Give the preparation type.
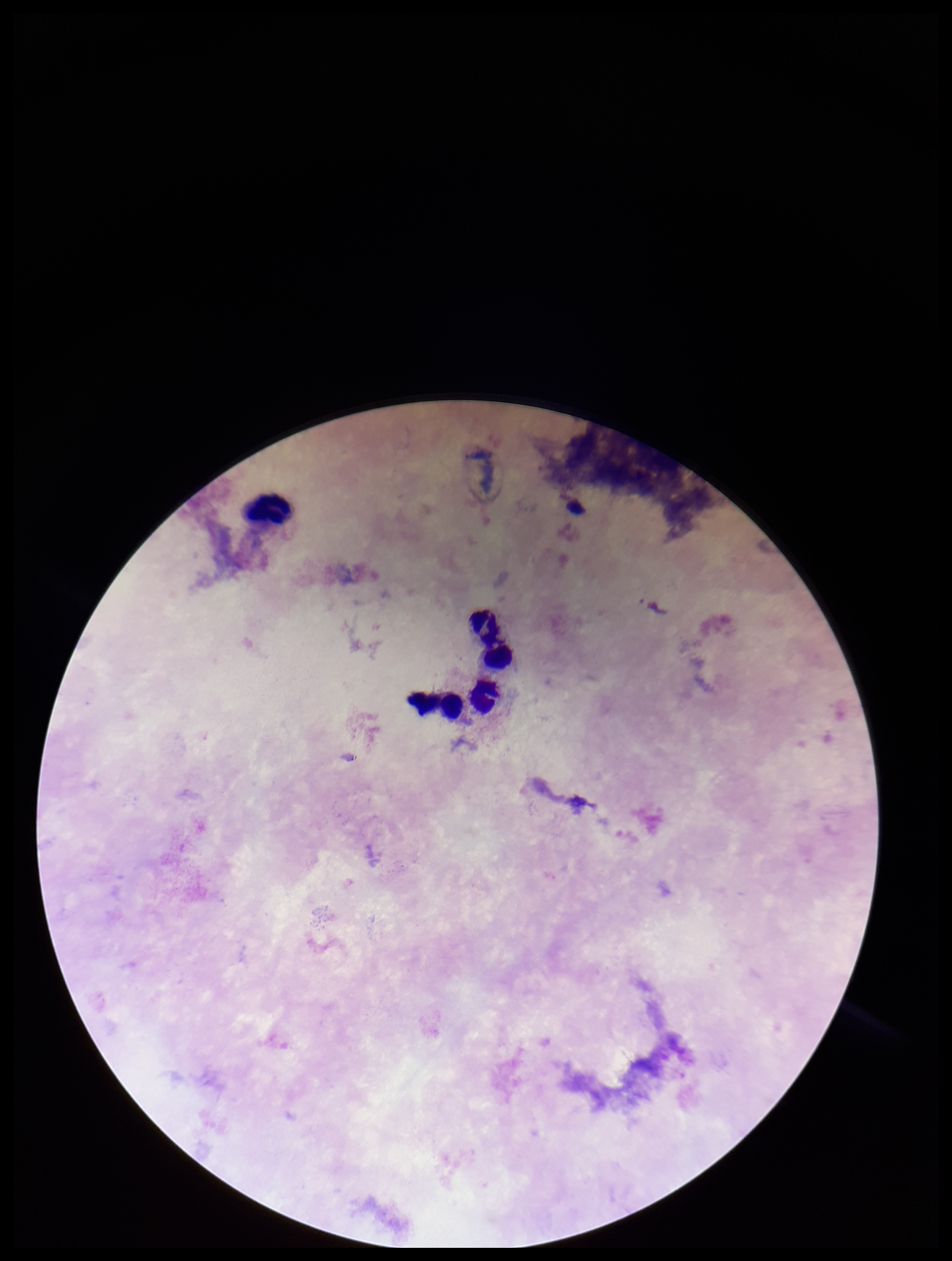

A thick smear.

parasite_count: 0
capture: smartphone photograph through the microscope eyepiece
field_of_view: single
image_size: 952×1261 pixels
plasmodium_parasites: none identified
leukocyte_count: 5
patient_malaria_status: negative
stain: Giemsa